State which parasite is depicted.
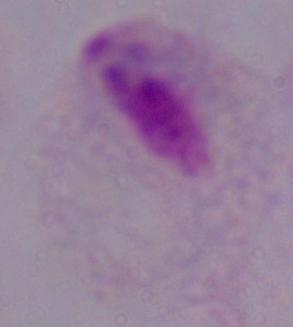

This is a trichomonad.

1000x magnification. Micrograph.